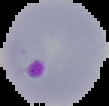
image size = 109×106 pixels
image type = segmented cell region with the area outside set to black
preparation = thin blood film
result = Plasmodium parasites detected